State which parasite is depicted.
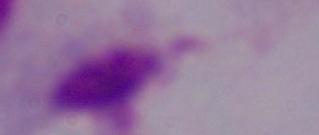
This is a trichomonad.

{
  "magnification": "1000x",
  "modality": "micrograph"
}